Outline each blood parasite and name the species.
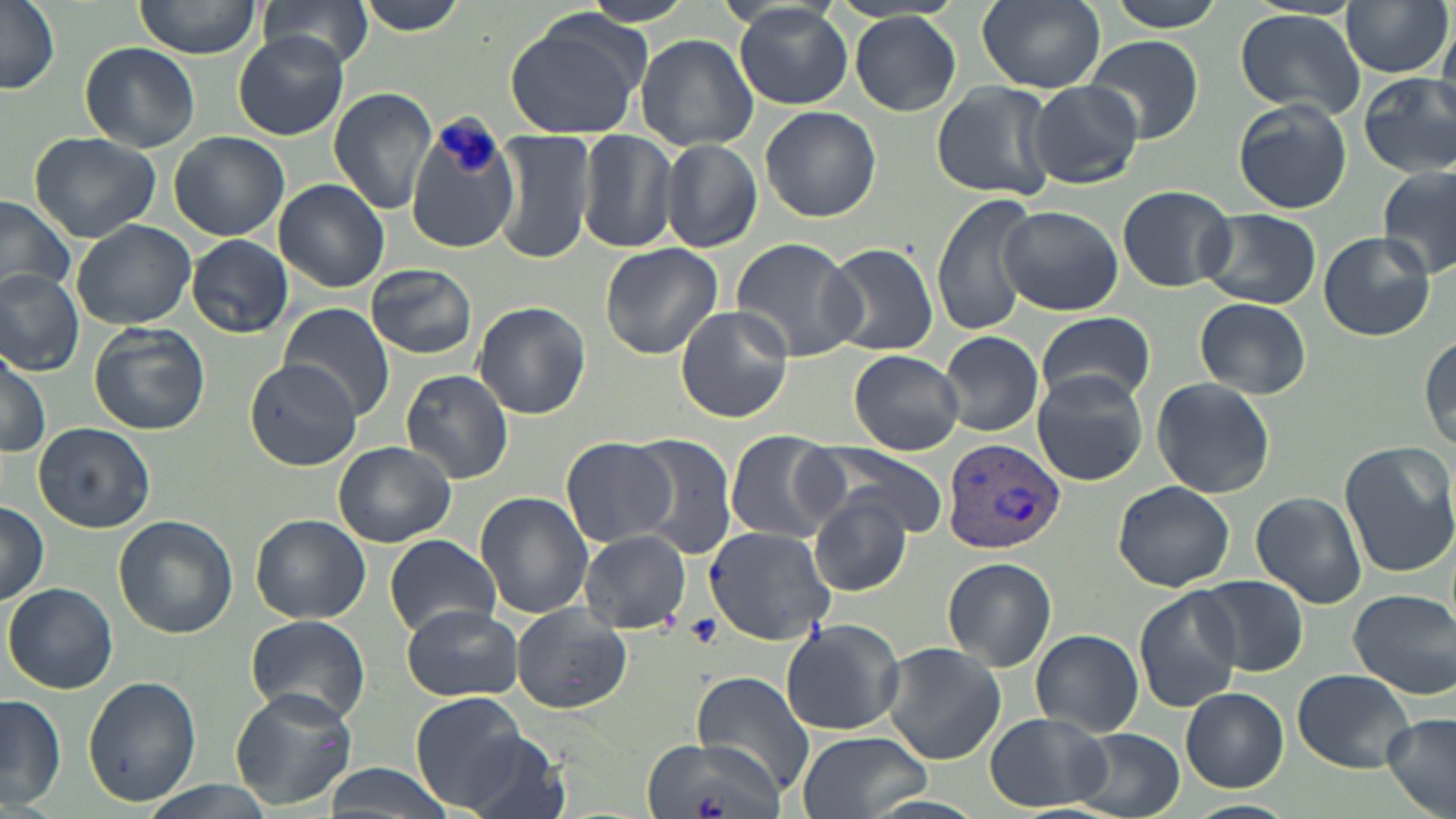

Approximate bounding boxes as [x1, y1, x2, y2] in pixels.
Plasmodium vivax-infected red blood cells: [941, 435, 1066, 555].
No Plasmodium falciparum, Plasmodium ovale, Plasmodium malariae, Babesia divergens, or Trypanosoma brucei observed.

{
  "slide_level_diagnosis": "Plasmodium vivax",
  "field_of_view": "single",
  "stain": "May-Grünwald-Giemsa",
  "magnification": "1000x",
  "preparation": "thin blood film",
  "uninfected_red_blood_cell_locations": "approximate bounding boxes as [x1, y1, x2, y2] in pixels: [0, 0, 61, 94], [132, 0, 263, 59], [259, 0, 375, 73], [355, 0, 471, 36], [572, 0, 699, 28], [977, 0, 1105, 91], [1103, 0, 1230, 32], [1339, 1, 1452, 77], [735, 5, 853, 110], [1235, 10, 1366, 117], [849, 12, 962, 116], [503, 13, 649, 140], [231, 33, 349, 141], [635, 34, 758, 151], [1081, 35, 1204, 144], [80, 41, 202, 152], [57, 46, 185, 237], [1358, 74, 1456, 179], [1025, 80, 1143, 189], [930, 82, 1057, 201], [328, 87, 438, 214], [1232, 99, 1352, 214], [760, 105, 882, 223], [405, 117, 518, 253], [168, 130, 288, 240], [492, 130, 595, 265], [575, 132, 676, 254], [29, 133, 161, 241], [661, 138, 761, 254], [1377, 163, 1455, 279], [273, 179, 391, 293], [1116, 184, 1238, 292], [931, 193, 1037, 337], [0, 194, 77, 301], [999, 206, 1124, 315], [1195, 208, 1321, 308], [72, 219, 197, 329], [1318, 231, 1436, 340], [187, 235, 293, 337], [729, 237, 862, 361], [599, 243, 723, 358], [822, 243, 938, 355], [366, 263, 478, 359], [0, 267, 85, 374], [1193, 297, 1311, 397], [473, 301, 591, 420], [282, 302, 396, 420], [675, 306, 795, 424], [1035, 310, 1155, 408], [88, 323, 211, 436], [938, 330, 1045, 437], [1419, 332, 1454, 457], [0, 345, 51, 459], [848, 350, 963, 454], [243, 357, 363, 470], [401, 368, 513, 483], [1030, 370, 1149, 485], [1150, 376, 1276, 500], [32, 422, 155, 533], [725, 431, 845, 543], [627, 434, 736, 557], [559, 437, 678, 547], [334, 440, 456, 546], [1339, 440, 1455, 579], [806, 443, 951, 541], [1113, 480, 1236, 592], [1250, 491, 1368, 610], [476, 492, 593, 616], [809, 496, 911, 594], [0, 502, 50, 606], [251, 513, 370, 622], [114, 515, 238, 641], [703, 526, 837, 644], [580, 531, 693, 635], [384, 535, 500, 637], [941, 557, 1058, 672], [1196, 577, 1309, 677], [5, 582, 118, 693], [1134, 587, 1243, 713], [1349, 588, 1455, 699], [402, 603, 522, 701], [511, 606, 631, 713], [243, 614, 371, 725], [779, 619, 907, 737], [1031, 629, 1143, 737], [880, 642, 1006, 765], [1292, 668, 1414, 772], [691, 671, 814, 794], [81, 675, 201, 807], [231, 684, 358, 809], [1181, 687, 1288, 792], [410, 692, 528, 808], [1, 694, 65, 809], [985, 713, 1108, 811], [1382, 714, 1456, 819], [1063, 729, 1183, 816], [796, 730, 931, 819], [460, 734, 570, 819], [646, 736, 786, 819], [322, 763, 451, 819], [142, 780, 271, 819], [1183, 799, 1296, 819]",
  "image_size": "1456×819 pixels",
  "platelet_locations": "approximate bounding boxes as [x1, y1, x2, y2] in pixels: [687, 614, 723, 647]",
  "modality": "light microscopy"
}